Locate every Plasmodium malariae-infected red blood cell.
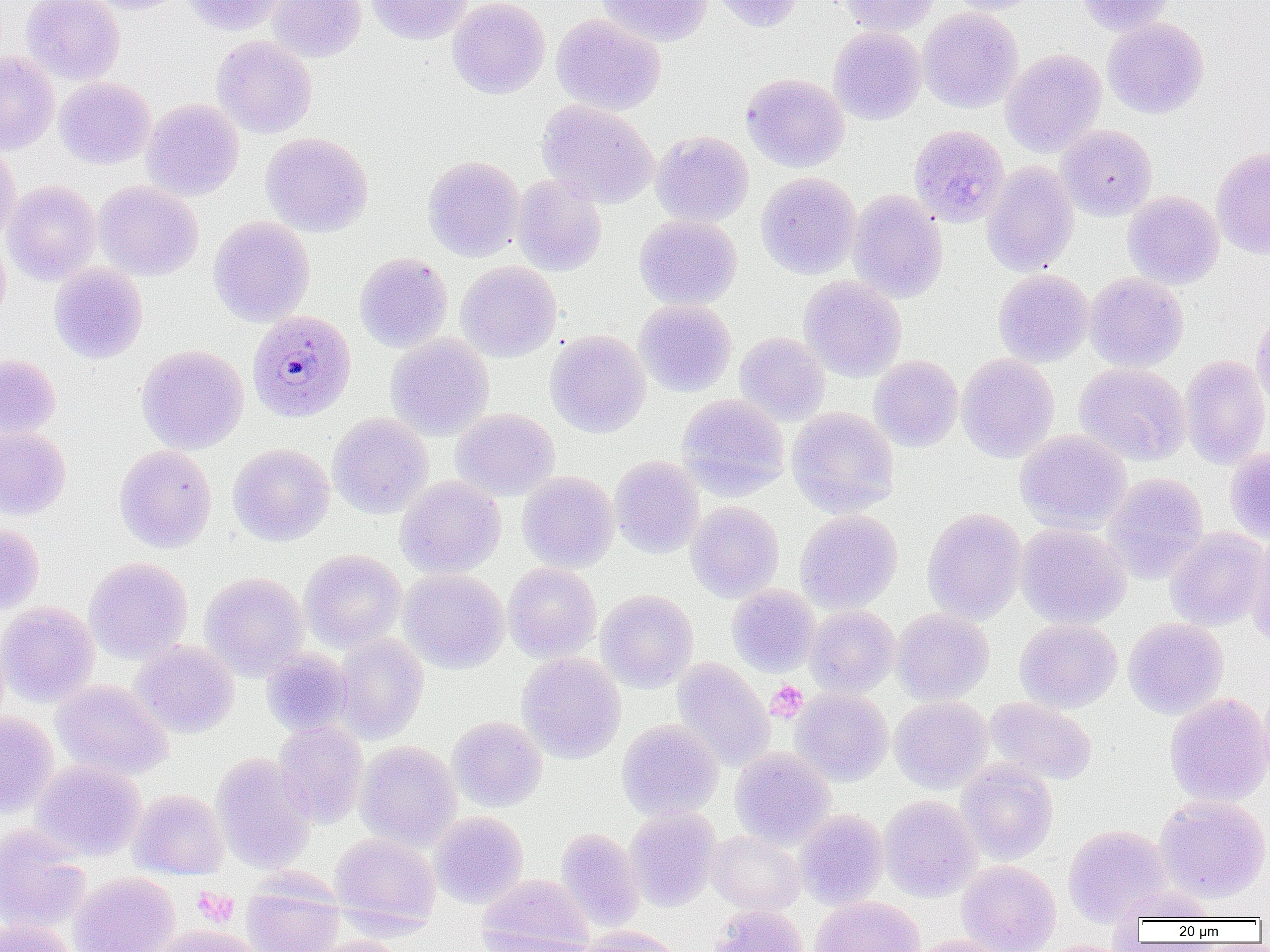
Approximate bounding boxes as named x1/y1/x2/y2 corners in pixels.
Plasmodium malariae-infected red blood cells: (x1=246, y1=310, x2=357, y2=423).

slide_level_diagnosis: Plasmodium malariae
modality: light microscopy
uninfected_red_blood_cell_locations: 'approximate bounding boxes as named x1/y1/x2/y2 corners in pixels: (x1=22, y1=0, x2=124, y2=85), (x1=82, y1=0, x2=189, y2=15), (x1=183, y1=0, x2=288, y2=36), (x1=267, y1=0, x2=366, y2=62), (x1=366, y1=0, x2=473, y2=45), (x1=447, y1=0, x2=549, y2=99), (x1=597, y1=0, x2=712, y2=47), (x1=709, y1=0, x2=805, y2=33), (x1=837, y1=0, x2=941, y2=37), (x1=945, y1=0, x2=1042, y2=15), (x1=1076, y1=0, x2=1174, y2=36), (x1=918, y1=7, x2=1023, y2=113), (x1=551, y1=14, x2=666, y2=115), (x1=1102, y1=17, x2=1208, y2=119), (x1=828, y1=26, x2=926, y2=124), (x1=212, y1=35, x2=317, y2=138), (x1=1001, y1=49, x2=1107, y2=157), (x1=0, y1=51, x2=59, y2=155), (x1=741, y1=73, x2=849, y2=172), (x1=54, y1=77, x2=155, y2=169), (x1=141, y1=98, x2=244, y2=201), (x1=537, y1=100, x2=659, y2=208), (x1=909, y1=124, x2=1009, y2=227), (x1=1057, y1=124, x2=1157, y2=220), (x1=651, y1=130, x2=753, y2=227), (x1=261, y1=132, x2=373, y2=236), (x1=0, y1=144, x2=21, y2=245), (x1=1211, y1=146, x2=1270, y2=259), (x1=423, y1=155, x2=525, y2=261), (x1=981, y1=161, x2=1079, y2=276), (x1=236, y1=172, x2=347, y2=287), (x1=756, y1=172, x2=861, y2=279), (x1=511, y1=174, x2=607, y2=276), (x1=3, y1=180, x2=101, y2=285), (x1=93, y1=180, x2=203, y2=281), (x1=847, y1=189, x2=948, y2=302), (x1=1123, y1=191, x2=1224, y2=289), (x1=634, y1=214, x2=742, y2=310), (x1=208, y1=216, x2=315, y2=326), (x1=0, y1=235, x2=11, y2=326), (x1=354, y1=252, x2=453, y2=352), (x1=455, y1=261, x2=562, y2=362), (x1=49, y1=262, x2=148, y2=363), (x1=993, y1=268, x2=1093, y2=367), (x1=1084, y1=272, x2=1188, y2=372), (x1=799, y1=276, x2=907, y2=382), (x1=635, y1=300, x2=737, y2=397), (x1=1250, y1=310, x2=1270, y2=411), (x1=545, y1=330, x2=650, y2=438), (x1=734, y1=332, x2=830, y2=425), (x1=386, y1=333, x2=494, y2=440), (x1=136, y1=344, x2=249, y2=454), (x1=957, y1=353, x2=1059, y2=463), (x1=0, y1=354, x2=61, y2=438), (x1=869, y1=355, x2=963, y2=451), (x1=1180, y1=355, x2=1270, y2=468), (x1=1074, y1=362, x2=1191, y2=465), (x1=677, y1=393, x2=789, y2=498), (x1=786, y1=407, x2=898, y2=517), (x1=450, y1=408, x2=559, y2=501), (x1=328, y1=413, x2=433, y2=519), (x1=0, y1=425, x2=71, y2=521), (x1=1015, y1=430, x2=1131, y2=533), (x1=228, y1=443, x2=334, y2=546), (x1=114, y1=445, x2=217, y2=553), (x1=1225, y1=446, x2=1270, y2=543), (x1=609, y1=456, x2=704, y2=558), (x1=517, y1=471, x2=619, y2=572), (x1=1102, y1=472, x2=1208, y2=585), (x1=395, y1=476, x2=506, y2=578), (x1=686, y1=501, x2=784, y2=602), (x1=922, y1=507, x2=1027, y2=624), (x1=795, y1=509, x2=902, y2=613), (x1=0, y1=522, x2=44, y2=614), (x1=1016, y1=523, x2=1131, y2=629), (x1=1165, y1=527, x2=1268, y2=631), (x1=1246, y1=530, x2=1270, y2=649), (x1=299, y1=549, x2=406, y2=652), (x1=84, y1=557, x2=193, y2=663), (x1=503, y1=562, x2=601, y2=663), (x1=399, y1=569, x2=510, y2=673), (x1=200, y1=572, x2=309, y2=679), (x1=726, y1=585, x2=821, y2=677), (x1=596, y1=589, x2=698, y2=692), (x1=0, y1=602, x2=99, y2=707), (x1=805, y1=605, x2=900, y2=697), (x1=892, y1=608, x2=994, y2=705), (x1=1123, y1=617, x2=1229, y2=719), (x1=1015, y1=618, x2=1122, y2=713), (x1=333, y1=632, x2=429, y2=744), (x1=130, y1=640, x2=239, y2=738), (x1=261, y1=648, x2=353, y2=737), (x1=517, y1=652, x2=626, y2=763), (x1=673, y1=658, x2=775, y2=771), (x1=52, y1=679, x2=172, y2=780), (x1=791, y1=688, x2=894, y2=785), (x1=1164, y1=693, x2=1270, y2=807), (x1=890, y1=696, x2=993, y2=793), (x1=985, y1=697, x2=1097, y2=785), (x1=0, y1=713, x2=58, y2=817), (x1=447, y1=716, x2=547, y2=812), (x1=617, y1=719, x2=723, y2=820), (x1=274, y1=720, x2=368, y2=828), (x1=355, y1=740, x2=462, y2=851), (x1=729, y1=747, x2=835, y2=848), (x1=211, y1=753, x2=316, y2=873), (x1=31, y1=759, x2=146, y2=861), (x1=956, y1=760, x2=1058, y2=864), (x1=129, y1=789, x2=228, y2=879), (x1=1155, y1=794, x2=1270, y2=902), (x1=879, y1=795, x2=981, y2=902), (x1=625, y1=807, x2=721, y2=911), (x1=795, y1=809, x2=889, y2=909), (x1=429, y1=811, x2=528, y2=909), (x1=0, y1=824, x2=91, y2=933), (x1=1063, y1=824, x2=1171, y2=926), (x1=556, y1=828, x2=645, y2=932), (x1=707, y1=831, x2=805, y2=915), (x1=330, y1=833, x2=440, y2=932), (x1=956, y1=860, x2=1061, y2=952), (x1=69, y1=872, x2=180, y2=952), (x1=477, y1=873, x2=593, y2=952), (x1=241, y1=874, x2=344, y2=952), (x1=1112, y1=885, x2=1215, y2=924), (x1=180, y1=887, x2=254, y2=934), (x1=810, y1=895, x2=925, y2=952), (x1=710, y1=905, x2=810, y2=952), (x1=0, y1=919, x2=79, y2=952), (x1=149, y1=925, x2=267, y2=952), (x1=578, y1=925, x2=683, y2=952), (x1=475, y1=931, x2=594, y2=952), (x1=909, y1=935, x2=1015, y2=952), (x1=305, y1=936, x2=411, y2=952), (x1=1026, y1=939, x2=1137, y2=952)'
magnification: 1000x
platelet_locations: 'approximate bounding boxes as named x1/y1/x2/y2 corners in pixels: (x1=766, y1=681, x2=807, y2=721), (x1=193, y1=888, x2=240, y2=926)'
image_size: 1270×952 pixels
field_of_view: one of a larger specimen
preparation: thin blood smear